Identify the preparation type.
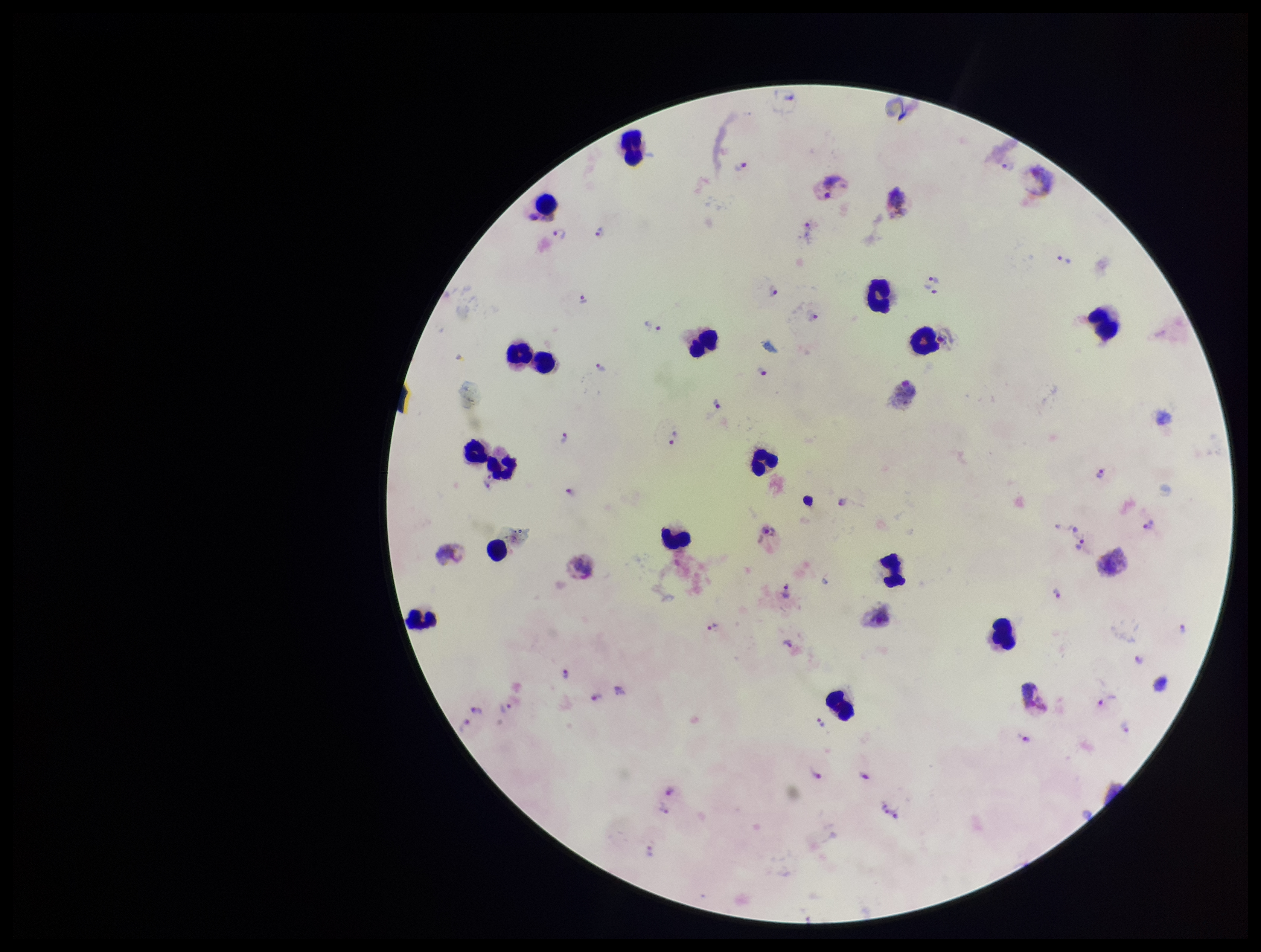

A thick smear.

Plasmodium parasites: detected. One field from this slide. Parasite count: 36. Photographed through the microscope eyepiece with a smartphone camera. Stained with Giemsa. Species reported for this patient: Plasmodium vivax. Patient malaria status: infected. Image is 1261×952 pixels. Leukocyte count: 17.